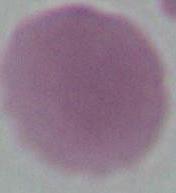
modality: photomicrograph
magnification: 1000x
identification: erythrocyte